Classify this cell by malaria status.
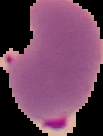
It is parasitized.

preparation = thin blood smear
image type = cell region segmented out of the field of view; surrounding area masked to black
image size = 103×136 pixels